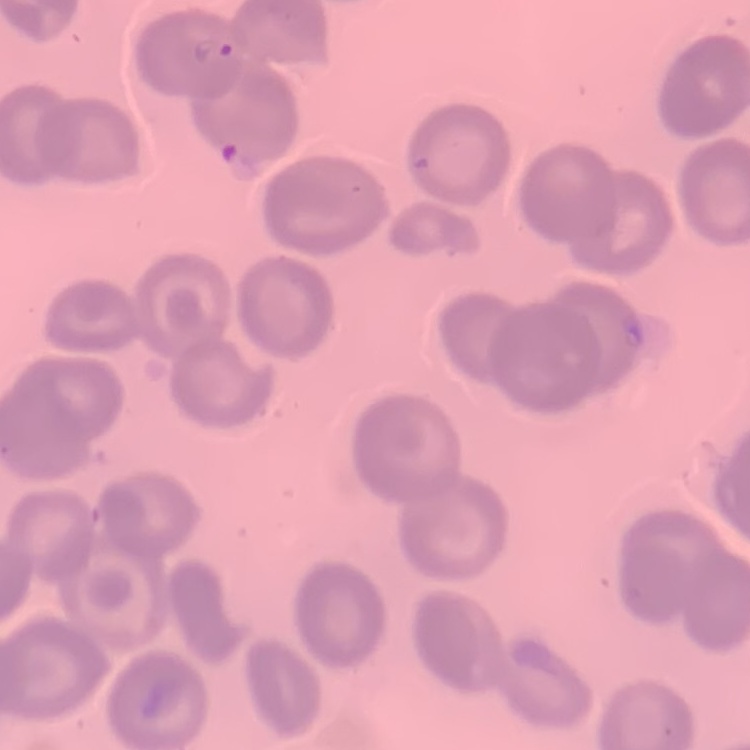

Summary:
  - Red blood cell morphology: no rouleaux formation
  - Preparation: thin peripheral smear
  - Image type: one tile cut from a larger photomicrograph
  - Stain: Field's or Giemsa